Outline each blood parasite and name the species.
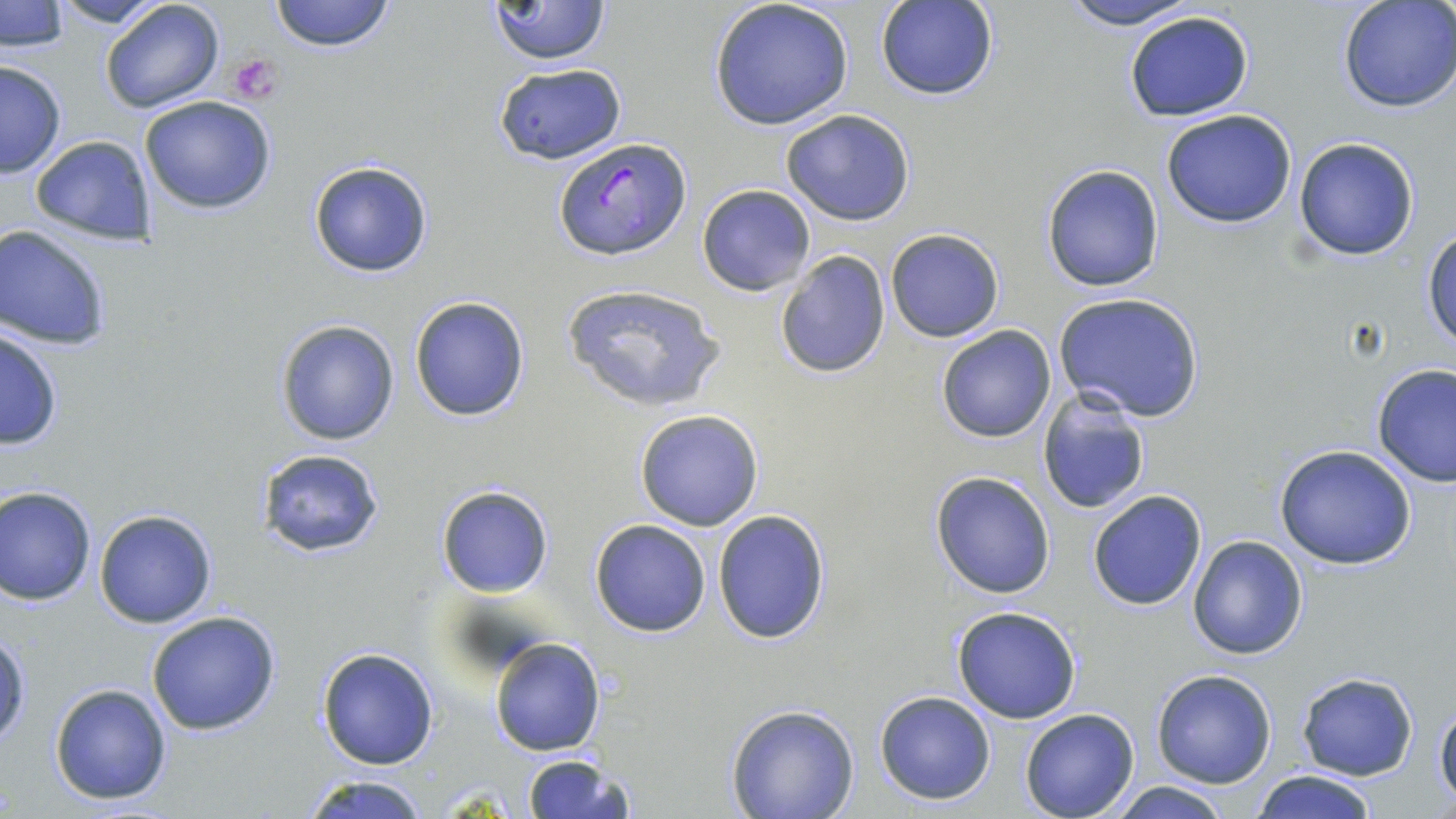
Approximate bounding boxes as [x1, y1, x2, y2] in pixels.
Plasmodium falciparum-infected red blood cells: [556, 136, 689, 261].
No Plasmodium ovale, Plasmodium malariae, Plasmodium vivax, Babesia divergens, or Trypanosoma brucei observed.

Platelet locations: [227, 53, 283, 104]. Uninfected red blood cell locations: [2, 0, 69, 51], [48, 0, 170, 28], [267, 0, 397, 53], [483, 0, 613, 66], [708, 0, 854, 130], [1056, 0, 1205, 29], [1336, 0, 1456, 114], [99, 1, 226, 115], [874, 1, 1000, 102], [1122, 10, 1255, 122], [0, 59, 67, 178], [495, 61, 624, 162], [493, 63, 625, 163], [138, 95, 279, 215], [780, 109, 916, 225], [1161, 109, 1298, 228], [29, 134, 159, 246], [1292, 136, 1421, 262], [309, 161, 433, 277], [1041, 163, 1165, 293], [697, 183, 816, 296], [0, 224, 113, 350], [1422, 227, 1456, 351], [885, 228, 1004, 342], [775, 249, 892, 379], [559, 283, 730, 415], [1052, 292, 1205, 422], [409, 295, 530, 421], [274, 318, 401, 446], [935, 324, 1056, 442], [1, 325, 65, 453], [1373, 364, 1456, 486], [1035, 388, 1151, 516], [634, 409, 764, 530], [1275, 445, 1420, 570], [258, 449, 385, 558], [931, 472, 1056, 597], [436, 485, 554, 598], [0, 486, 98, 606], [1086, 491, 1208, 611], [93, 510, 218, 627], [711, 510, 831, 646], [589, 519, 712, 637], [1187, 535, 1308, 659], [951, 605, 1082, 723], [146, 609, 282, 736], [1, 631, 32, 751], [489, 638, 605, 756], [317, 646, 438, 769], [1151, 670, 1276, 788], [1297, 671, 1418, 780], [49, 682, 174, 804], [875, 691, 997, 805], [1433, 700, 1456, 806], [725, 705, 861, 819], [1019, 709, 1140, 819], [520, 752, 635, 819], [1251, 769, 1377, 819], [300, 772, 432, 819], [1107, 780, 1233, 819]. Slide-level diagnosis: Plasmodium falciparum. May-Grünwald-Giemsa-stained preparation. Thin blood smear. Single field of view. Light microscopy. Image is 1456×819 pixels. Captured at 1000x magnification.